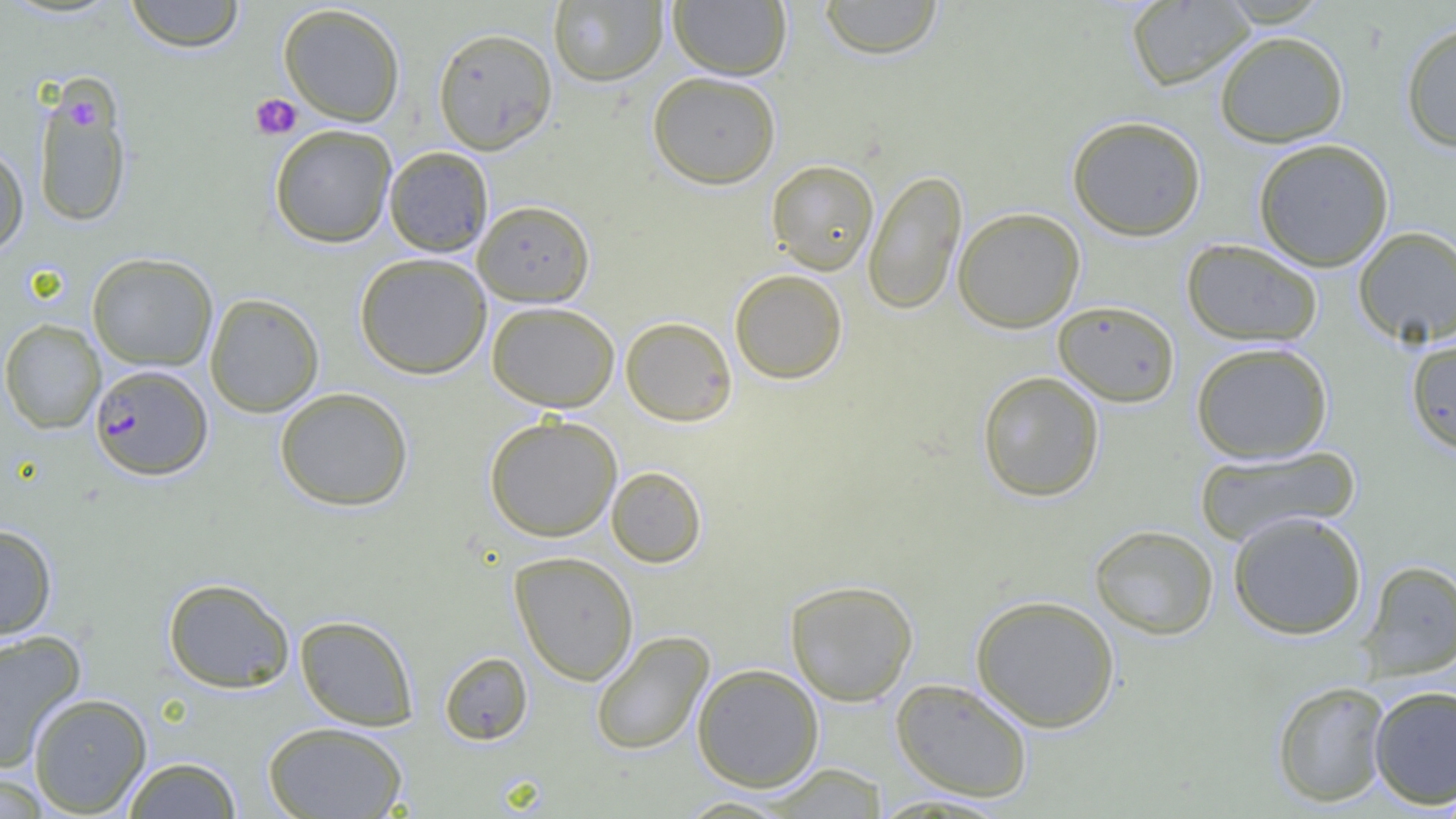
Summary:
  - Coordinate format: approximate bounding boxes as (x1,y1)-(x2,y2) corner pairs in pixels
  - Plasmodium falciparum-infected red blood cell locations: (89,364)-(212,481)
  - Platelet locations: (250,94)-(302,140), (69,100)-(101,127)
  - Uninfected red blood cell locations: (125,0)-(245,52), (548,0)-(668,87), (668,0)-(792,80), (818,0)-(944,59), (1126,1)-(1256,91), (278,3)-(406,127), (1400,20)-(1456,153), (432,26)-(558,155), (1214,30)-(1349,148), (647,70)-(781,189), (32,76)-(133,229), (1066,115)-(1207,240), (269,124)-(397,248), (1253,138)-(1394,271), (0,142)-(29,256), (384,146)-(494,257), (766,159)-(879,275), (863,169)-(967,316), (473,200)-(595,307), (952,207)-(1085,333), (1353,226)-(1456,347), (1181,239)-(1323,346), (87,252)-(218,371), (354,252)-(492,379), (729,268)-(848,384), (205,293)-(324,417), (1053,300)-(1180,407), (486,301)-(620,412), (620,316)-(737,426), (0,319)-(106,434), (1405,335)-(1456,454), (1190,341)-(1333,464), (977,371)-(1105,501), (274,387)-(414,512), (483,414)-(622,542), (1192,446)-(1361,546), (606,466)-(707,568), (1227,510)-(1368,640), (0,524)-(58,641), (1089,524)-(1219,640), (509,551)-(639,685), (1358,559)-(1456,681), (162,577)-(295,693), (784,579)-(919,706), (970,594)-(1121,732), (294,615)-(419,731), (590,630)-(714,756), (0,631)-(87,772), (439,651)-(533,745), (691,663)-(825,792), (890,678)-(1033,802), (1271,680)-(1392,807), (1368,684)-(1456,810), (28,693)-(152,816), (263,721)-(409,819), (122,757)-(242,818), (762,764)-(890,817), (0,772)-(52,818), (867,792)-(1014,816), (674,795)-(798,817)
  - Slide-level diagnosis: Plasmodium falciparum
  - Preparation: thin blood film
  - Magnification: 1000x
  - Modality: optical microscopy
  - Field of view: one of a larger specimen
  - Image size: 1456×819 pixels